Give the preparation type.
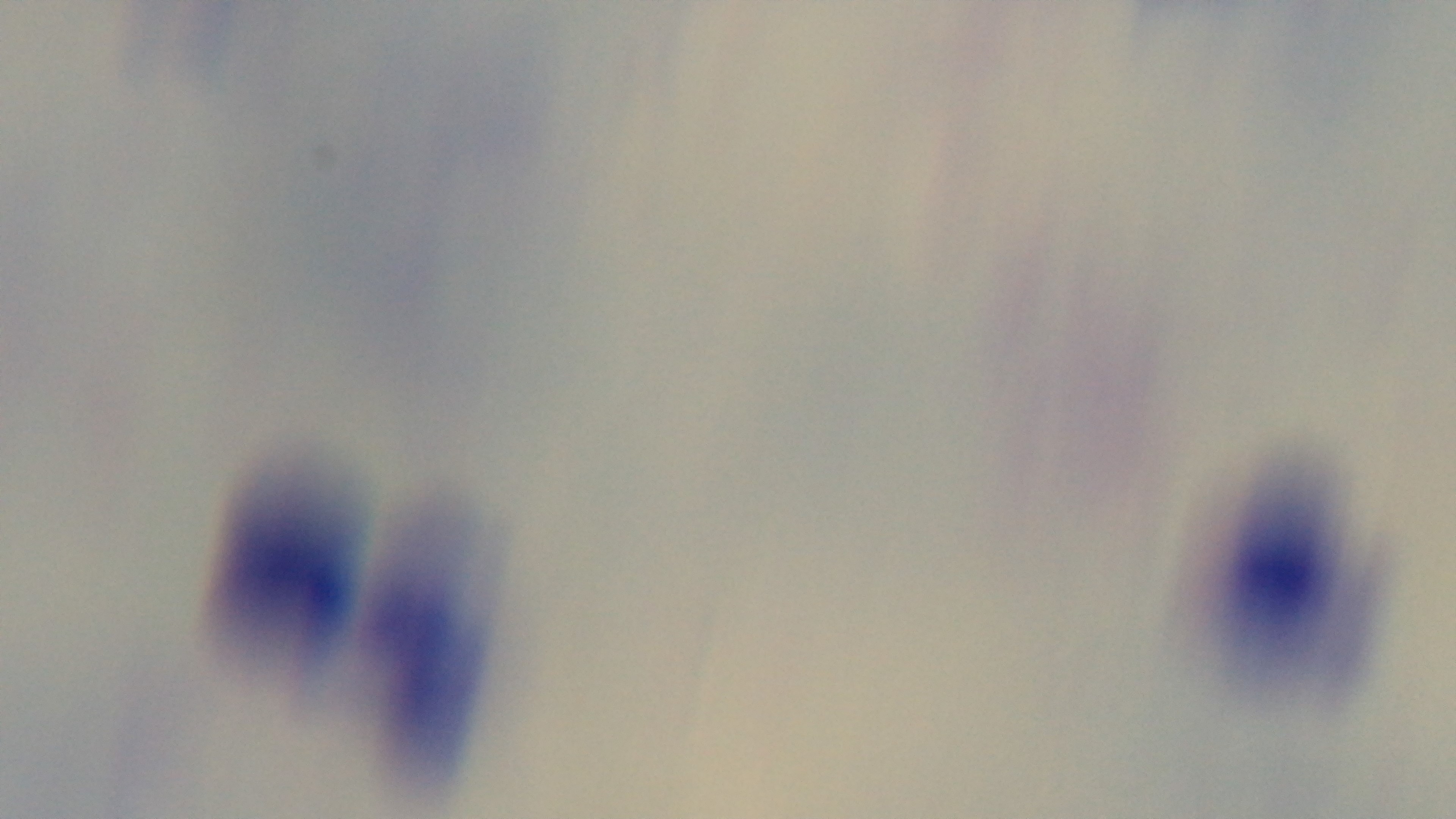
A thick smear.

stain: Giemsa
modality: light microscopy
malaria_status: uninfected
field_of_view: single
objective: 100x oil immersion
capture: mounted 4K digital camera